Classify this cell by malaria status.
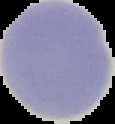
It is uninfected.

Image is 115×124 pixels. From a thin blood smear. Segmented cell region on a black background.